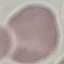

Summary:
  - Malaria status: uninfected
  - Stain: Giemsa
  - Image type: automatically extracted cell patch, resized to 64 × 64 pixels
  - Preparation: thin blood film
  - Capture: smartphone camera at the microscope eyepiece